Outline each Plasmodium vivax-infected red blood cell.
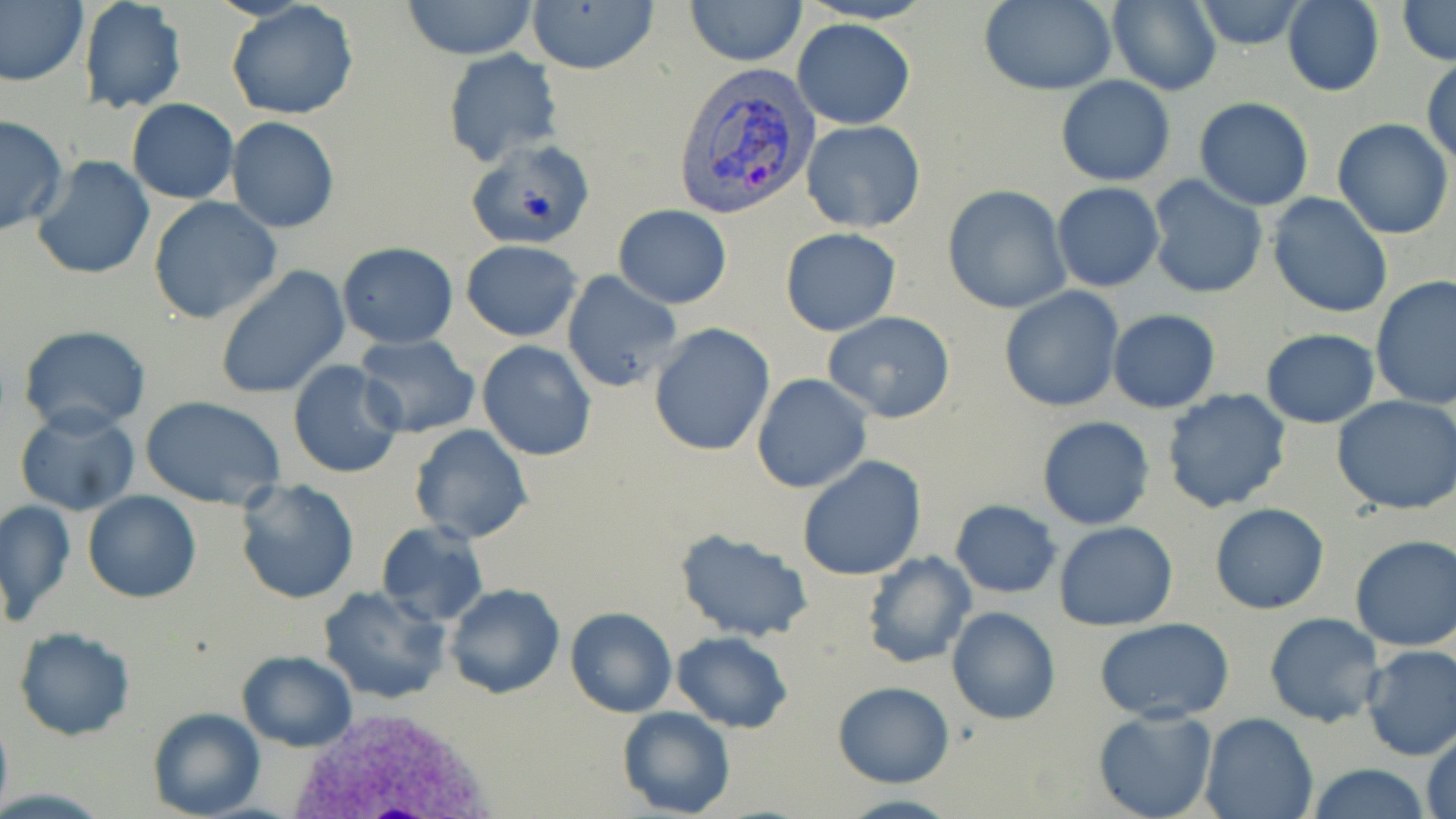

Approximate bounding boxes as (x1, y1, x2, y2) in pixels.
Plasmodium vivax-infected red blood cells: (672, 62, 817, 223).

slide-level diagnosis = Plasmodium vivax
image size = 1456×819 pixels
field of view = one of a larger specimen
uninfected red blood cell locations = approximate bounding boxes as (x1, y1, x2, y2) in pixels: (77, 0, 186, 115), (686, 0, 803, 66), (795, 0, 937, 24), (1106, 0, 1222, 95), (1193, 0, 1309, 50), (1395, 0, 1456, 66), (0, 1, 88, 87), (225, 1, 359, 121), (400, 1, 539, 59), (527, 1, 659, 75), (976, 1, 1118, 95), (1282, 1, 1384, 96), (793, 19, 914, 129), (442, 50, 564, 167), (1424, 60, 1455, 164), (1056, 76, 1175, 185), (1194, 98, 1313, 210), (127, 99, 239, 203), (0, 116, 68, 235), (226, 117, 340, 233), (1332, 118, 1453, 240), (802, 121, 926, 233), (467, 142, 598, 251), (30, 153, 157, 281), (1146, 176, 1268, 300), (1051, 182, 1164, 292), (942, 185, 1070, 314), (1267, 192, 1395, 318), (148, 196, 282, 324), (614, 204, 732, 308), (585, 211, 719, 376), (780, 227, 902, 336), (461, 239, 583, 341), (336, 243, 458, 348), (215, 267, 350, 399), (561, 269, 684, 394), (1370, 277, 1456, 409), (999, 287, 1125, 412), (1108, 310, 1220, 413), (823, 312, 956, 423), (647, 321, 773, 455), (19, 325, 151, 435), (1261, 327, 1379, 429), (353, 334, 481, 438), (476, 341, 596, 461), (288, 360, 407, 479), (752, 374, 871, 493), (1162, 388, 1292, 514), (141, 395, 288, 508), (1332, 395, 1456, 515), (13, 404, 141, 517), (1037, 416, 1153, 530), (410, 425, 533, 544), (797, 456, 926, 580), (234, 479, 359, 604), (82, 491, 201, 604), (0, 499, 75, 626), (949, 500, 1062, 598), (1210, 502, 1330, 615), (375, 521, 488, 627), (1055, 521, 1178, 630), (676, 529, 813, 642), (1349, 535, 1456, 650), (863, 552, 976, 671), (444, 584, 564, 700), (318, 585, 449, 705), (946, 605, 1060, 725), (566, 607, 677, 716), (1264, 612, 1385, 727), (1095, 617, 1237, 724), (13, 627, 135, 741), (672, 629, 793, 732), (1360, 644, 1456, 761), (237, 650, 356, 751), (832, 680, 954, 787), (1091, 706, 1219, 819), (0, 707, 12, 819), (147, 707, 264, 819), (617, 707, 737, 819), (1200, 713, 1319, 819), (1422, 727, 1456, 819), (1302, 760, 1431, 819)
modality = light microscopy
stain = May-Grünwald-Giemsa
platelet locations = approximate bounding boxes as (x1, y1, x2, y2) in pixels: (520, 186, 557, 224)
white blood cell locations = approximate bounding boxes as (x1, y1, x2, y2) in pixels: (274, 701, 503, 817)
magnification = 1000x
preparation = thin blood smear